Classify this cell by malaria status.
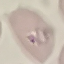
Parasitized.

Automatically extracted cell patch, resized to 64 × 64 pixels. Giemsa stain. Acquired by smartphone through the microscope eyepiece. Thin blood film.